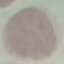
malaria status = uninfected
image type = automatically extracted cell patch, resized to 64 × 64 pixels
capture = smartphone camera at the microscope eyepiece
stain = Giemsa
preparation = thin blood smear